Outline each uninfected red blood cell.
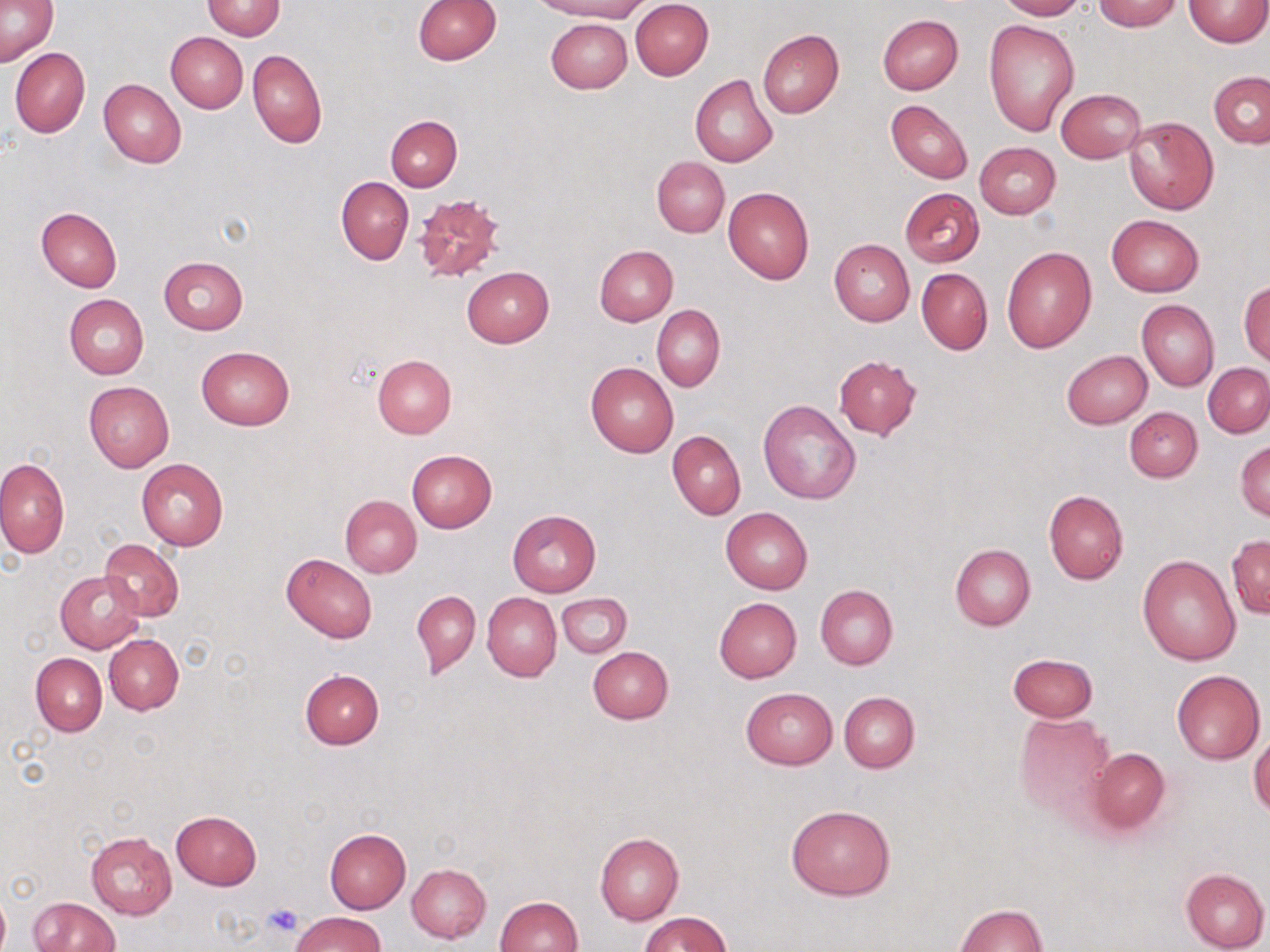
Approximate bounding boxes as (x1,y1)-(x2,y2) corner pairs in pixels.
Uninfected red blood cells: (413,0)-(501,64), (540,0)-(649,21), (630,0)-(714,80), (995,0)-(1086,20), (1093,0)-(1181,31), (1184,0)-(1268,46), (1,1)-(59,68), (201,1)-(285,40), (877,15)-(963,95), (546,19)-(632,93), (983,19)-(1079,135), (756,28)-(843,119), (166,32)-(248,113), (9,48)-(91,138), (247,49)-(327,148), (1208,70)-(1270,149), (690,75)-(779,168), (98,79)-(187,168), (1056,88)-(1146,163), (887,100)-(972,184), (386,115)-(462,191), (1123,115)-(1219,215), (974,142)-(1061,218), (652,156)-(729,237), (336,176)-(413,265), (723,187)-(814,285), (899,187)-(984,266), (412,191)-(507,282), (36,207)-(123,292), (1107,214)-(1204,297), (829,239)-(915,326), (594,246)-(678,326), (1001,246)-(1097,352), (158,256)-(248,335), (462,268)-(554,347), (917,268)-(992,354), (1239,281)-(1269,367), (63,294)-(149,379), (1137,300)-(1219,390), (653,305)-(725,392), (196,344)-(295,431), (1062,350)-(1152,428), (372,354)-(456,438), (833,354)-(922,440), (585,362)-(679,457), (1203,363)-(1270,438), (84,381)-(173,470), (758,398)-(861,504), (1125,407)-(1202,482), (668,430)-(746,520), (1235,441)-(1270,522), (406,450)-(497,532), (0,458)-(69,560), (136,459)-(228,550), (1044,491)-(1128,584), (340,495)-(422,578), (721,507)-(813,594), (507,510)-(601,596), (1227,534)-(1270,619), (99,539)-(183,621), (950,544)-(1035,631), (281,553)-(378,643), (1137,554)-(1241,664), (55,570)-(144,653), (815,585)-(897,669), (412,590)-(480,679), (482,592)-(560,681), (557,593)-(632,658), (715,597)-(802,682), (104,634)-(183,714), (588,648)-(673,724), (1007,652)-(1098,722), (30,653)-(107,736), (300,669)-(385,749), (1171,669)-(1265,764), (741,687)-(837,768), (838,692)-(919,774), (1015,712)-(1116,822), (1249,732)-(1270,817), (1087,747)-(1172,835), (787,805)-(895,899), (170,810)-(263,889), (325,827)-(411,912), (85,831)-(177,920), (594,832)-(683,924), (407,863)-(491,942), (1181,868)-(1269,952), (0,892)-(10,952), (495,896)-(582,952), (29,897)-(118,951), (953,903)-(1047,952), (641,911)-(731,951), (292,912)-(387,952).

Summary:
  - Platelet locations: (262,902)-(304,939)
  - Slide-level diagnosis: negative for blood parasites
  - Modality: optical microscopy
  - Image size: 1270×952 pixels
  - Preparation: thin blood film
  - Stain: May-Grünwald-Giemsa
  - Magnification: 1000x
  - Field of view: single